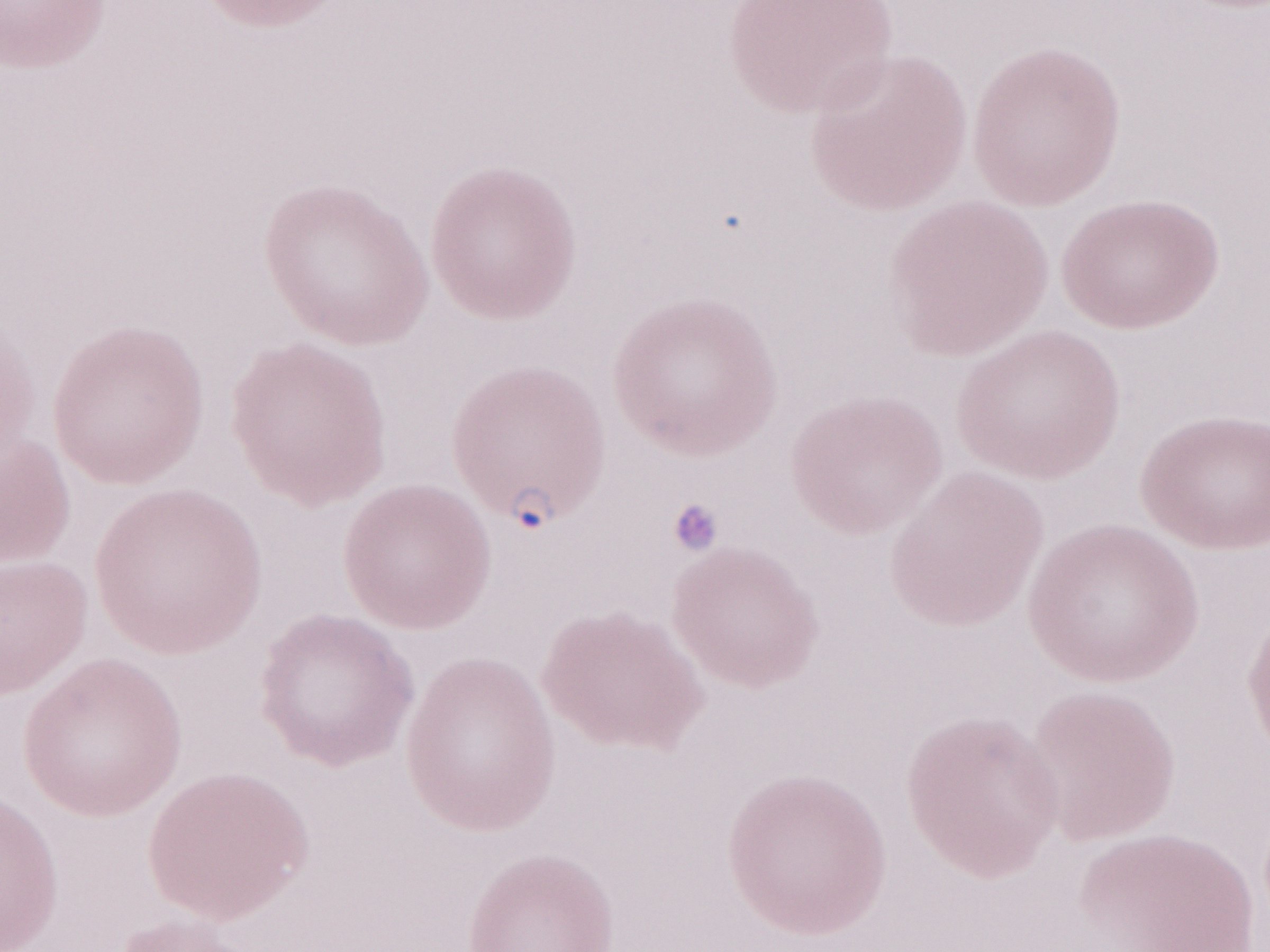 May-Grünwald-Giemsa (MGG) stain. Olympus BX43 microscope, Olympus DP73 camera. Image is 1270×952 pixels. Magnification: 1,000x. Single field of view. Thin peripheral-blood smear. Patient-level malaria diagnosis: positive.